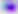
Summary:
  - Identification: Toxoplasma gondii
  - Magnification: 400x
  - Modality: micrograph